Name the cell type shown.
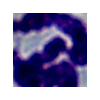

This is a leukocyte.

Micrograph. Captured at 1000x magnification.